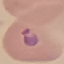
Malaria status: parasitized. Cell patch, automatically extracted from a larger field of view and resized to 64 × 64 pixels. Giemsa stain. Thin blood smear. Photographed with a smartphone camera at the microscope eyepiece.